Classify this cell by malaria status.
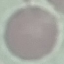
Uninfected.

preparation = thin smear
stain = Giemsa
image type = automatically extracted cell patch, resized to 64 × 64 pixels
capture = smartphone through the microscope eyepiece